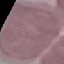

Summary:
  - Result: no malaria parasites seen
  - Stain: Giemsa
  - Preparation: thin blood film
  - Capture: smartphone camera at the microscope eyepiece
  - Image type: cell patch, automatically extracted from a larger field of view and resized to 64 × 64 pixels